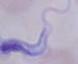
Summary:
  - Modality: micrograph
  - Magnification: 1000x
  - Identification: trypanosome